Outline each uninfected red blood cell.
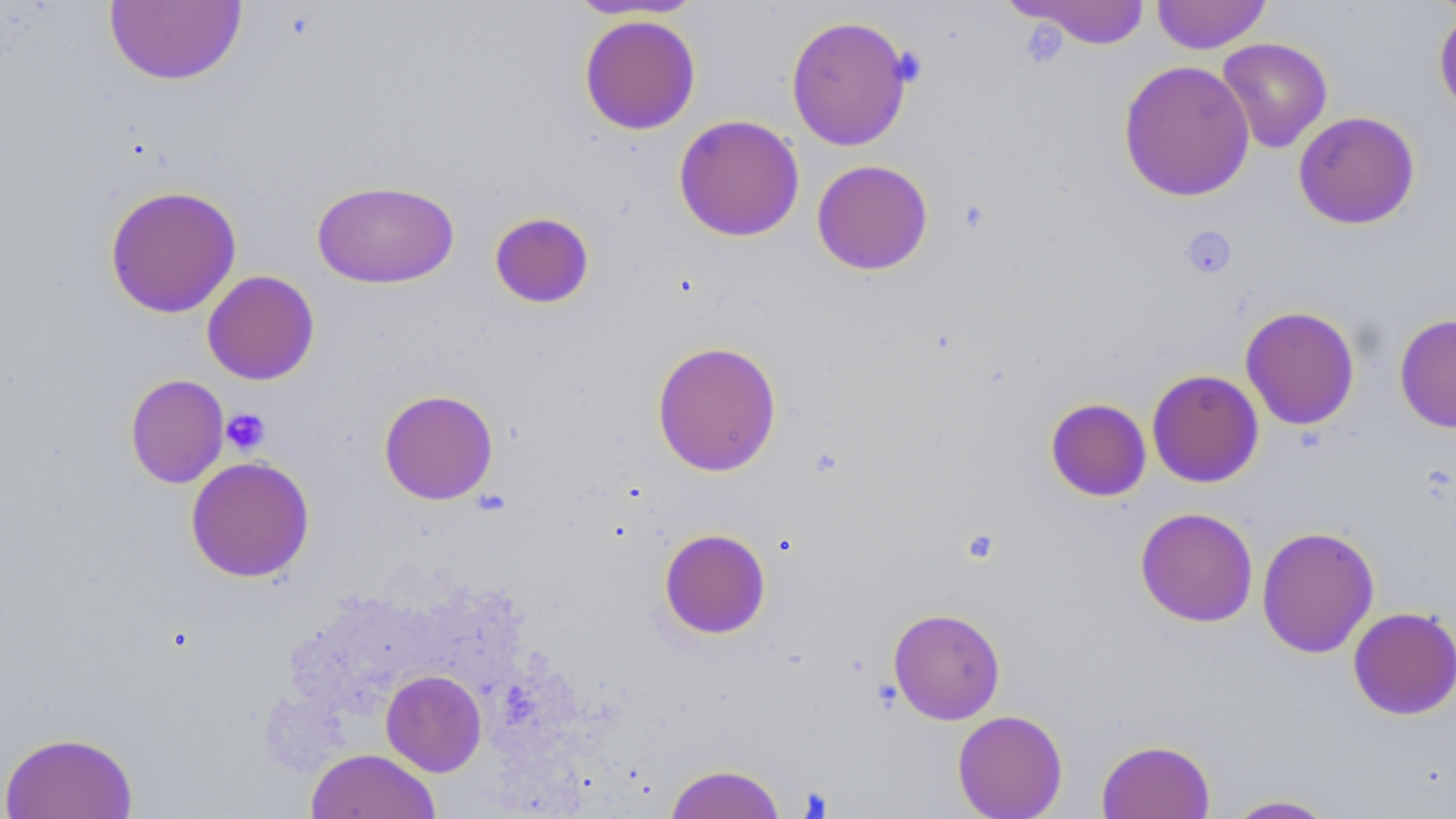

Approximate bounding boxes as [x1, y1, x2, y2] in pixels.
Uninfected red blood cells: [564, 0, 704, 20], [1152, 0, 1272, 54], [104, 1, 247, 85], [1008, 1, 1152, 49], [1433, 9, 1456, 121], [579, 14, 701, 135], [786, 15, 913, 151], [1216, 37, 1332, 153], [1118, 60, 1255, 202], [1293, 111, 1420, 229], [673, 114, 805, 242], [811, 159, 933, 275], [311, 179, 459, 289], [104, 184, 242, 318], [489, 211, 595, 309], [201, 270, 320, 385], [1240, 305, 1360, 430], [1394, 313, 1456, 433], [651, 340, 782, 477], [1146, 369, 1264, 488], [125, 374, 229, 489], [379, 389, 499, 505], [1045, 397, 1151, 502], [186, 455, 315, 582], [1135, 507, 1259, 627], [1256, 525, 1380, 658], [658, 528, 771, 639], [1347, 606, 1456, 720], [888, 607, 1006, 724], [381, 669, 487, 776], [952, 709, 1068, 819], [1, 732, 139, 818], [1096, 739, 1215, 819], [306, 748, 441, 819], [664, 763, 786, 819], [1221, 794, 1340, 818].

Platelet locations: [1182, 226, 1237, 279], [221, 409, 270, 455]. Slide-level diagnosis: no evidence of blood parasites. Light microscopy. May-Grünwald-Giemsa stain. 1000x magnification. Image is 1456×819 pixels. Thin blood smear. Single field of view.